Classify this cell by malaria status.
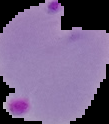

It is parasitized.

image_size: 109×124 pixels
preparation: thin blood smear
image_type: segmented cell region on a black background